Locate every Plasmodium parasite.
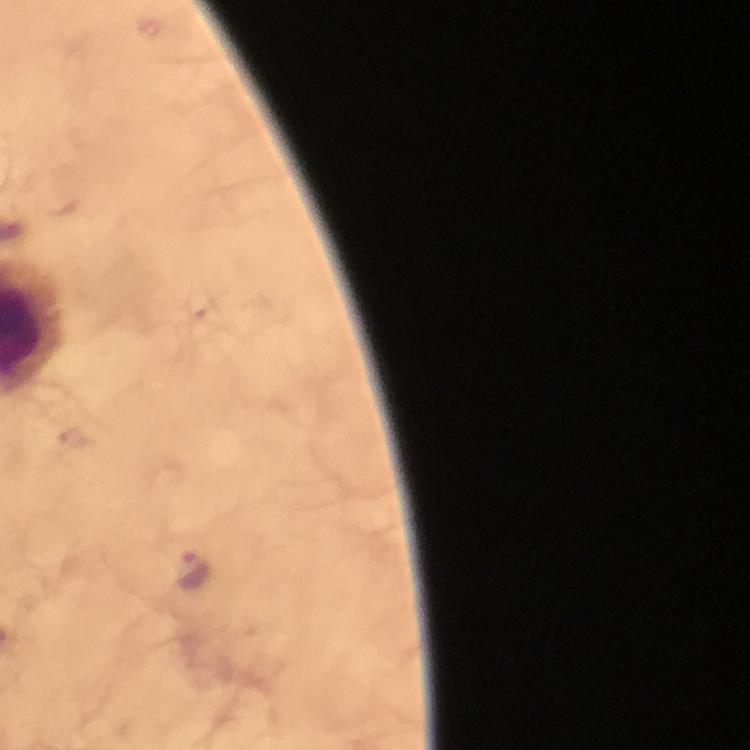

Approximate centers as (x, y) in pixels.
Plasmodium parasites: (74, 439), (193, 571).

At 100x magnification. Giemsa-stained preparation. Immersion oil applied. Photographed with a smartphone mounted on the microscope. Image is 750×750 pixels. Cropped region of a single field of view. From a malaria diagnostic workup. Thick smear.